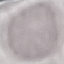

Result: no malaria parasites seen. Cell patch, automatically extracted from a larger field of view and resized to 64 × 64 pixels. Thin blood film. Acquired by smartphone through the microscope eyepiece. Giemsa-stained preparation.